Point out each leukocyte.
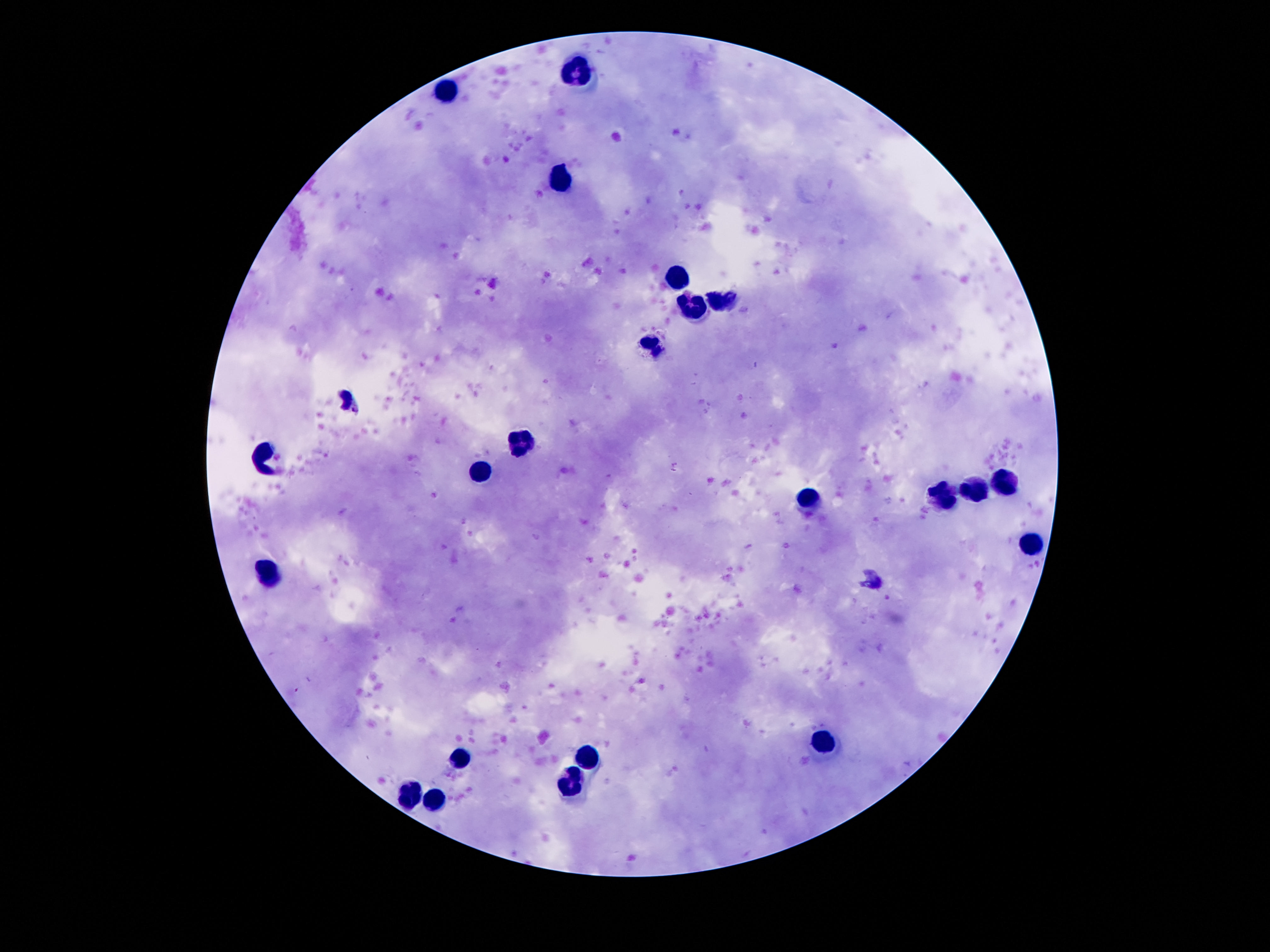

Approximate object centers, in pixels from the top-left corner.
Leukocytes: (x=581, y=74), (x=448, y=89), (x=559, y=176), (x=675, y=275), (x=721, y=300), (x=694, y=305), (x=653, y=346), (x=520, y=443), (x=266, y=457), (x=481, y=472), (x=1005, y=485), (x=975, y=490), (x=944, y=496), (x=809, y=500), (x=1030, y=545), (x=270, y=575), (x=823, y=744), (x=460, y=756), (x=585, y=760), (x=571, y=785), (x=411, y=793), (x=434, y=797).

Smartphone photograph taken through the microscope eyepiece. Single field of view. Image is 1270×952 pixels. Giemsa-stained preparation. Thick blood film. Patient malaria status: not infected. 100x magnification.